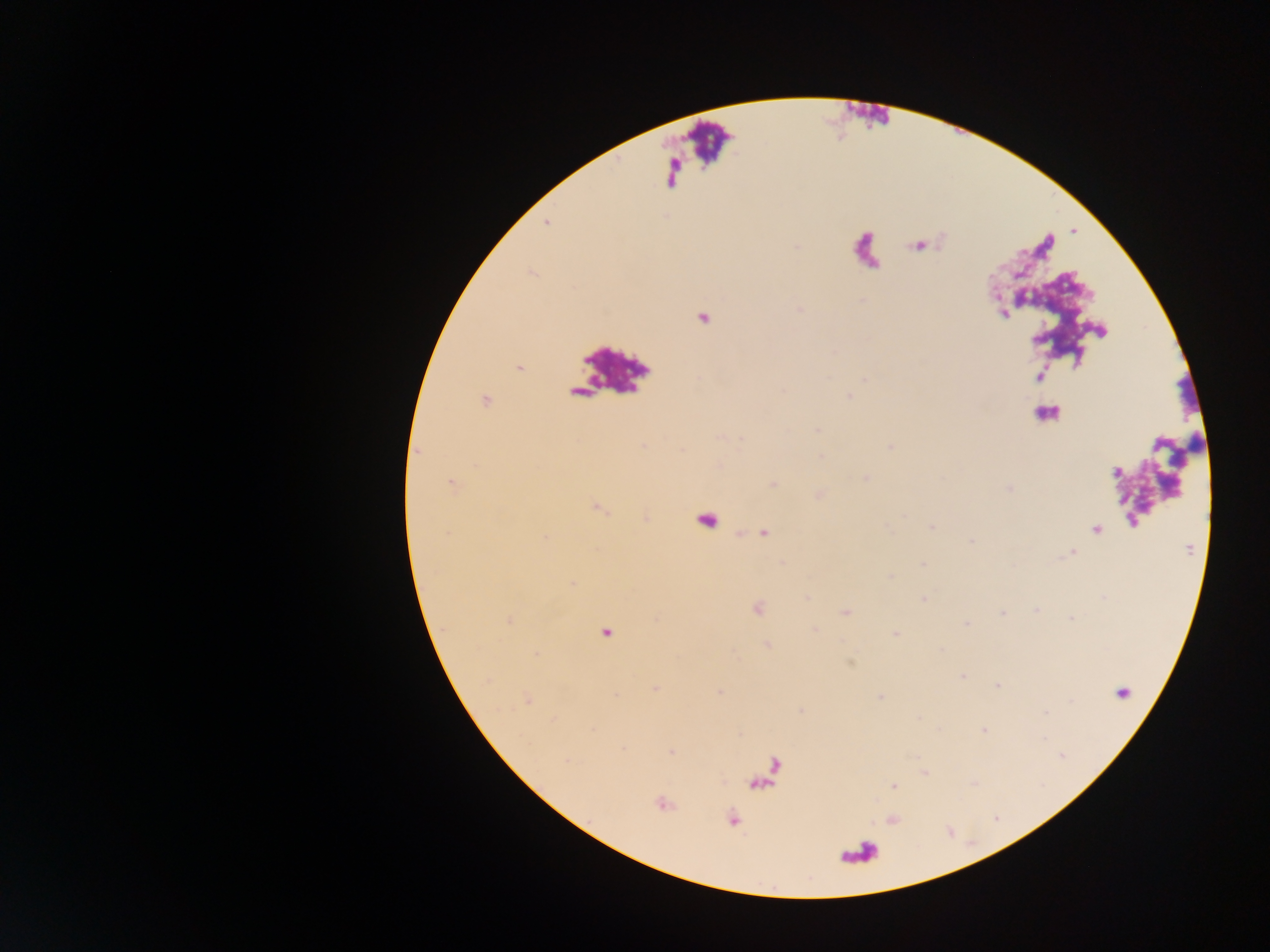 Approximate centers as x y in pixels. Malaria parasite locations: 519 368; 485 400; 450 482; 1096 530; 606 633; 963 675; 654 688; 672 751; 567 761; 893 786; 732 819. Sample from Ghana. Single field of view. Mobile-phone photograph taken through the microscope. Thick blood film. Image is 1270×952 pixels.